Locate every blood parasite and identify its species.
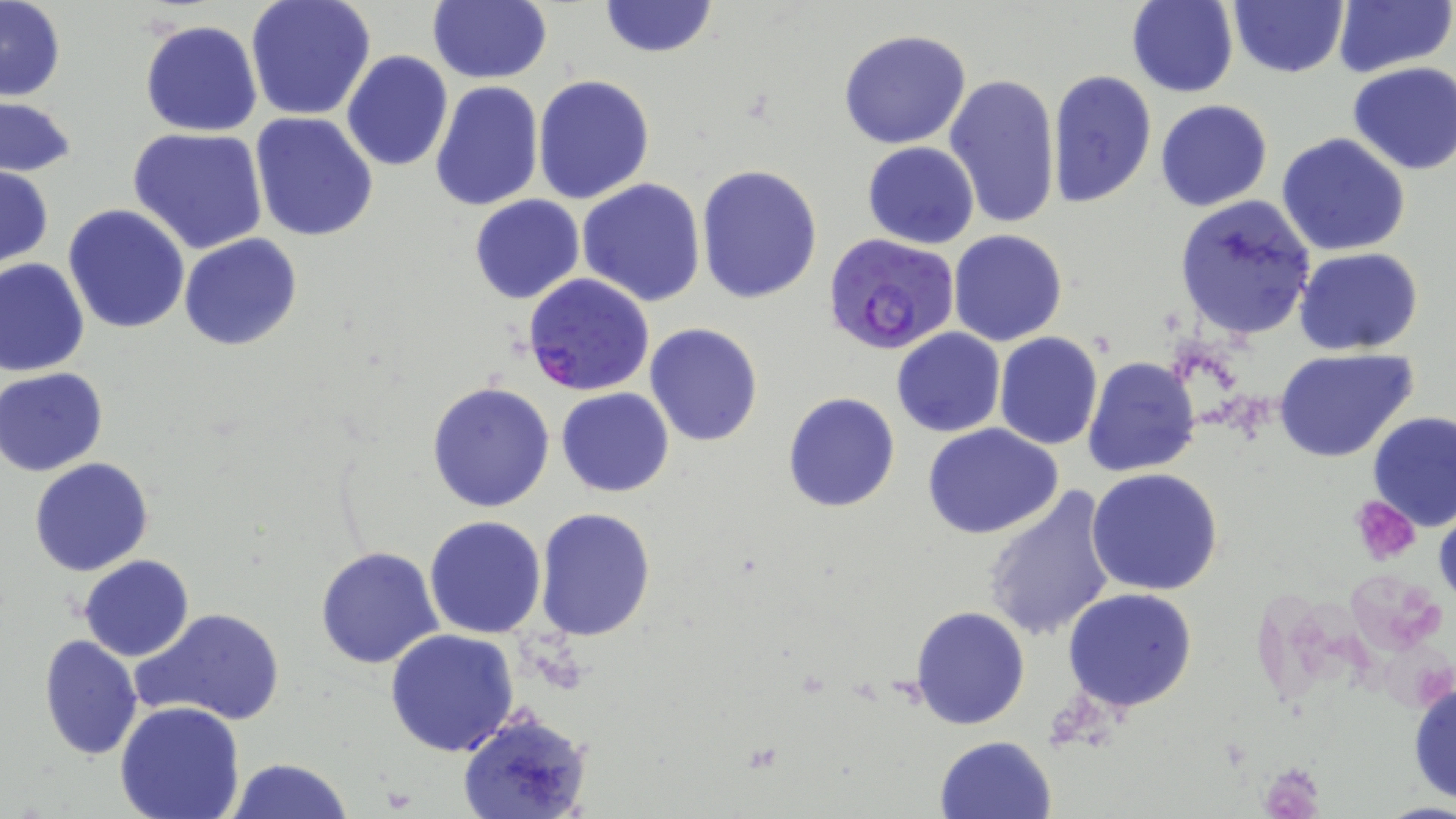
Approximate bounding boxes as named x1/y1/x2/y2 corners in pixels.
Plasmodium falciparum-infected red blood cells: (x1=821, y1=235, x2=963, y2=353), (x1=522, y1=272, x2=655, y2=396).
No Plasmodium ovale, Plasmodium malariae, Plasmodium vivax, Babesia divergens, or Trypanosoma brucei observed.

Summary:
  - Platelet locations: (x1=1349, y1=495, x2=1421, y2=566)
  - Uninfected red blood cell locations: (x1=1, y1=0, x2=66, y2=102), (x1=245, y1=0, x2=376, y2=122), (x1=598, y1=0, x2=717, y2=59), (x1=1125, y1=1, x2=1239, y2=97), (x1=1228, y1=1, x2=1347, y2=78), (x1=1335, y1=1, x2=1452, y2=77), (x1=426, y1=2, x2=552, y2=85), (x1=139, y1=20, x2=263, y2=138), (x1=838, y1=28, x2=972, y2=150), (x1=341, y1=50, x2=452, y2=172), (x1=1346, y1=62, x2=1456, y2=174), (x1=1045, y1=70, x2=1158, y2=211), (x1=943, y1=72, x2=1060, y2=229), (x1=532, y1=75, x2=656, y2=206), (x1=429, y1=80, x2=543, y2=213), (x1=0, y1=97, x2=76, y2=178), (x1=1154, y1=99, x2=1273, y2=212), (x1=250, y1=113, x2=378, y2=242), (x1=127, y1=127, x2=268, y2=254), (x1=1277, y1=133, x2=1412, y2=257), (x1=863, y1=141, x2=979, y2=249), (x1=695, y1=164, x2=822, y2=305), (x1=0, y1=165, x2=53, y2=270), (x1=577, y1=179, x2=705, y2=306), (x1=470, y1=195, x2=585, y2=303), (x1=1173, y1=197, x2=1317, y2=341), (x1=63, y1=204, x2=192, y2=334), (x1=949, y1=229, x2=1068, y2=346), (x1=178, y1=234, x2=303, y2=351), (x1=1294, y1=248, x2=1423, y2=354), (x1=0, y1=257, x2=91, y2=376), (x1=644, y1=322, x2=764, y2=446), (x1=891, y1=328, x2=1005, y2=438), (x1=994, y1=332, x2=1104, y2=451), (x1=1273, y1=349, x2=1421, y2=463), (x1=1082, y1=355, x2=1201, y2=478), (x1=1, y1=367, x2=109, y2=476), (x1=427, y1=381, x2=554, y2=512), (x1=556, y1=388, x2=673, y2=496), (x1=782, y1=390, x2=900, y2=512), (x1=1367, y1=410, x2=1456, y2=530), (x1=922, y1=424, x2=1064, y2=539), (x1=29, y1=458, x2=154, y2=576), (x1=1086, y1=468, x2=1223, y2=595), (x1=979, y1=485, x2=1119, y2=643), (x1=1433, y1=503, x2=1456, y2=617), (x1=534, y1=508, x2=657, y2=643), (x1=424, y1=516, x2=547, y2=638), (x1=315, y1=545, x2=444, y2=670), (x1=80, y1=555, x2=193, y2=661), (x1=1062, y1=589, x2=1200, y2=712), (x1=909, y1=605, x2=1030, y2=731), (x1=129, y1=606, x2=287, y2=727), (x1=384, y1=629, x2=520, y2=756), (x1=38, y1=634, x2=142, y2=761), (x1=1408, y1=675, x2=1456, y2=807), (x1=114, y1=700, x2=246, y2=819), (x1=455, y1=710, x2=591, y2=819), (x1=934, y1=735, x2=1057, y2=819), (x1=227, y1=758, x2=353, y2=819)
  - Slide-level diagnosis: Plasmodium falciparum
  - Modality: optical microscopy
  - Field of view: one of a larger specimen
  - Magnification: 1000x
  - Preparation: thin blood film
  - Image size: 1456×819 pixels
  - Stain: May-Grünwald-Giemsa